Assess this cell for malaria.
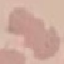

Uninfected.

image_type: automatically extracted cell patch, resized to 64 × 64 pixels
capture: smartphone through the microscope eyepiece
preparation: thin smear
stain: Giemsa